Describe the morphology of the erythrocytes.
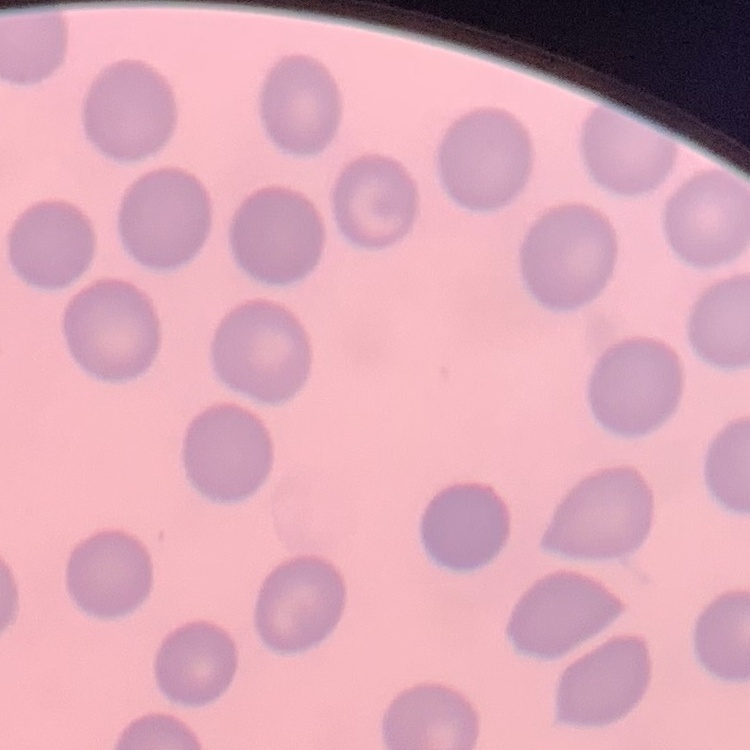
No rouleaux formation.

Square crop of a larger photomicrograph. Thin peripheral smear. Stained with either Field's or Giemsa.